Identify the cell.
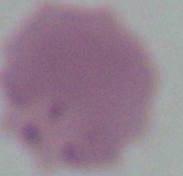
This is an erythrocyte.

Summary:
  - Magnification: 1000x
  - Modality: micrograph